Name the blood parasite species.
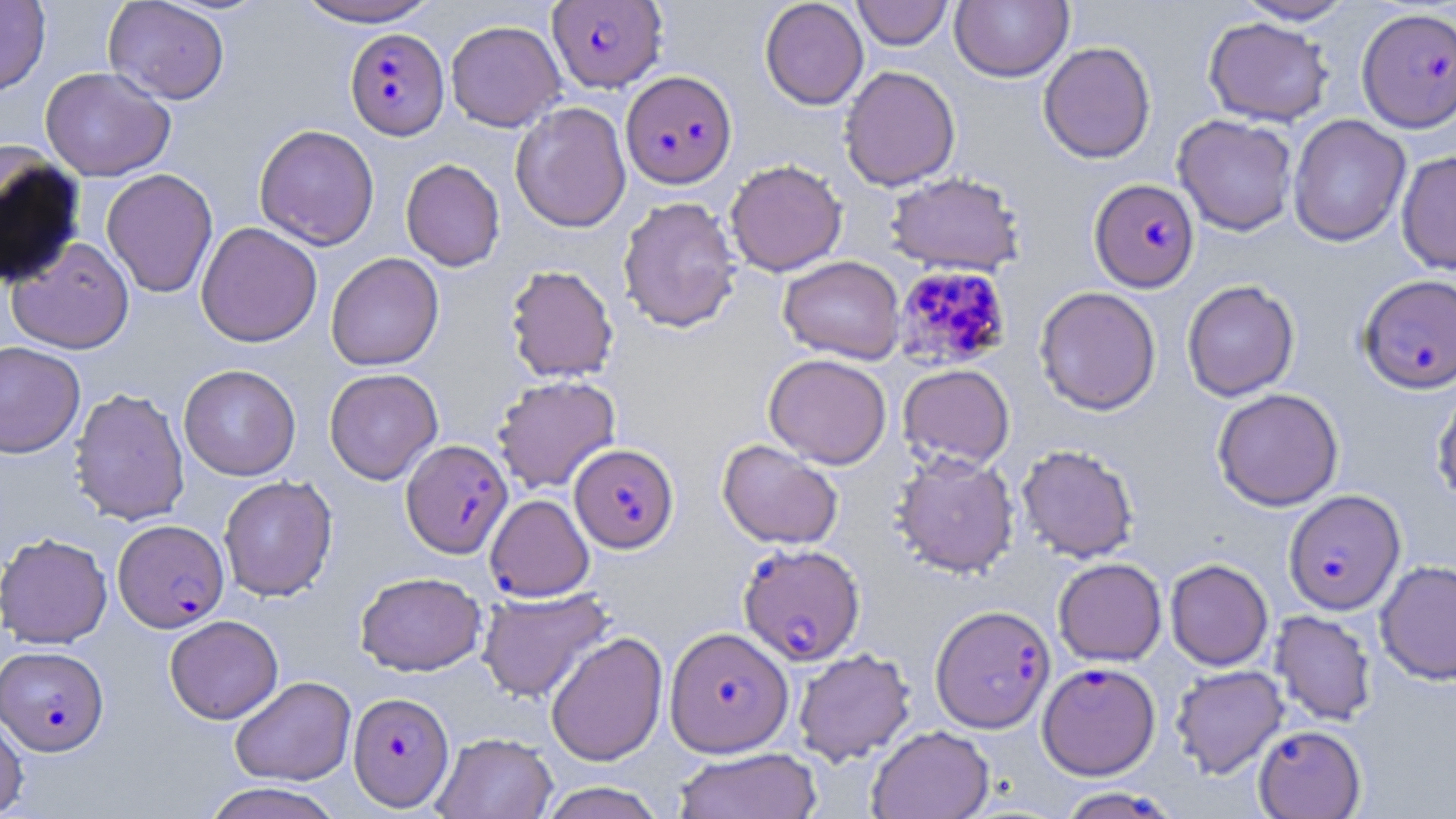
Plasmodium falciparum.

stain = May-Grünwald-Giemsa
Plasmodium falciparum-infected red blood cell locations = approximate bounding boxes as named x1/y1/x2/y2 corners in pixels: (x1=547, y1=0, x2=667, y2=92), (x1=1357, y1=6, x2=1456, y2=133), (x1=345, y1=28, x2=449, y2=141), (x1=621, y1=70, x2=738, y2=189), (x1=1088, y1=178, x2=1201, y2=292), (x1=893, y1=265, x2=1012, y2=371), (x1=1357, y1=274, x2=1456, y2=395), (x1=401, y1=439, x2=513, y2=558), (x1=569, y1=443, x2=679, y2=553), (x1=1283, y1=489, x2=1405, y2=615), (x1=485, y1=494, x2=594, y2=601), (x1=113, y1=519, x2=228, y2=632), (x1=738, y1=543, x2=865, y2=666), (x1=930, y1=604, x2=1055, y2=733), (x1=665, y1=626, x2=794, y2=757), (x1=0, y1=645, x2=109, y2=756), (x1=1038, y1=661, x2=1161, y2=780), (x1=348, y1=692, x2=454, y2=810), (x1=1253, y1=725, x2=1366, y2=818), (x1=1055, y1=786, x2=1181, y2=818)
uninfected red blood cell locations = approximate bounding boxes as named x1/y1/x2/y2 corners in pixels: (x1=0, y1=0, x2=51, y2=96), (x1=292, y1=0, x2=442, y2=27), (x1=760, y1=0, x2=869, y2=110), (x1=851, y1=0, x2=953, y2=50), (x1=1234, y1=0, x2=1357, y2=25), (x1=103, y1=1, x2=230, y2=104), (x1=950, y1=1, x2=1073, y2=82), (x1=1203, y1=17, x2=1333, y2=127), (x1=446, y1=20, x2=565, y2=132), (x1=1038, y1=41, x2=1156, y2=164), (x1=839, y1=65, x2=961, y2=191), (x1=40, y1=66, x2=175, y2=181), (x1=510, y1=101, x2=631, y2=233), (x1=1172, y1=114, x2=1298, y2=236), (x1=1287, y1=114, x2=1411, y2=246), (x1=254, y1=124, x2=380, y2=250), (x1=0, y1=145, x2=85, y2=287), (x1=1396, y1=151, x2=1456, y2=274), (x1=401, y1=158, x2=505, y2=271), (x1=725, y1=159, x2=848, y2=276), (x1=101, y1=168, x2=218, y2=298), (x1=885, y1=172, x2=1026, y2=276), (x1=617, y1=196, x2=742, y2=334), (x1=196, y1=222, x2=322, y2=347), (x1=7, y1=236, x2=135, y2=354), (x1=326, y1=252, x2=444, y2=371), (x1=778, y1=256, x2=905, y2=364), (x1=505, y1=264, x2=619, y2=383), (x1=1182, y1=279, x2=1300, y2=402), (x1=1034, y1=286, x2=1162, y2=415), (x1=0, y1=340, x2=86, y2=458), (x1=764, y1=353, x2=892, y2=469), (x1=179, y1=364, x2=301, y2=480), (x1=898, y1=364, x2=1015, y2=470), (x1=324, y1=368, x2=443, y2=485), (x1=492, y1=374, x2=621, y2=494), (x1=1431, y1=384, x2=1456, y2=508), (x1=69, y1=387, x2=190, y2=526), (x1=1212, y1=388, x2=1344, y2=511), (x1=717, y1=439, x2=843, y2=549), (x1=1016, y1=444, x2=1140, y2=563), (x1=891, y1=451, x2=1020, y2=579), (x1=218, y1=475, x2=338, y2=601), (x1=1, y1=532, x2=112, y2=649), (x1=1053, y1=558, x2=1167, y2=666), (x1=1165, y1=559, x2=1273, y2=671), (x1=1375, y1=560, x2=1456, y2=685), (x1=355, y1=571, x2=486, y2=676), (x1=476, y1=588, x2=614, y2=703), (x1=1270, y1=610, x2=1377, y2=726), (x1=165, y1=615, x2=283, y2=724), (x1=545, y1=631, x2=668, y2=766), (x1=793, y1=648, x2=915, y2=765), (x1=1171, y1=665, x2=1289, y2=779), (x1=230, y1=675, x2=356, y2=786), (x1=0, y1=709, x2=29, y2=818), (x1=867, y1=725, x2=994, y2=819), (x1=432, y1=732, x2=557, y2=819), (x1=672, y1=747, x2=821, y2=819), (x1=200, y1=782, x2=347, y2=819), (x1=536, y1=782, x2=667, y2=819)
image size = 1456×819 pixels
preparation = thin blood smear
modality = optical microscopy
magnification = 1000x
field of view = single